Report the malaria status of this cell.
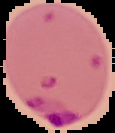
Parasitized.

Summary:
  - Image size: 115×133 pixels
  - Preparation: thin blood smear
  - Image type: segmented cell region with the area outside set to black